Report the malaria status of this cell.
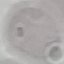
Uninfected.

{
  "stain": "Giemsa",
  "capture": "smartphone camera at the microscope eyepiece",
  "preparation": "thin smear",
  "image_type": "automatically extracted cell patch, resized to 64 × 64 pixels"
}